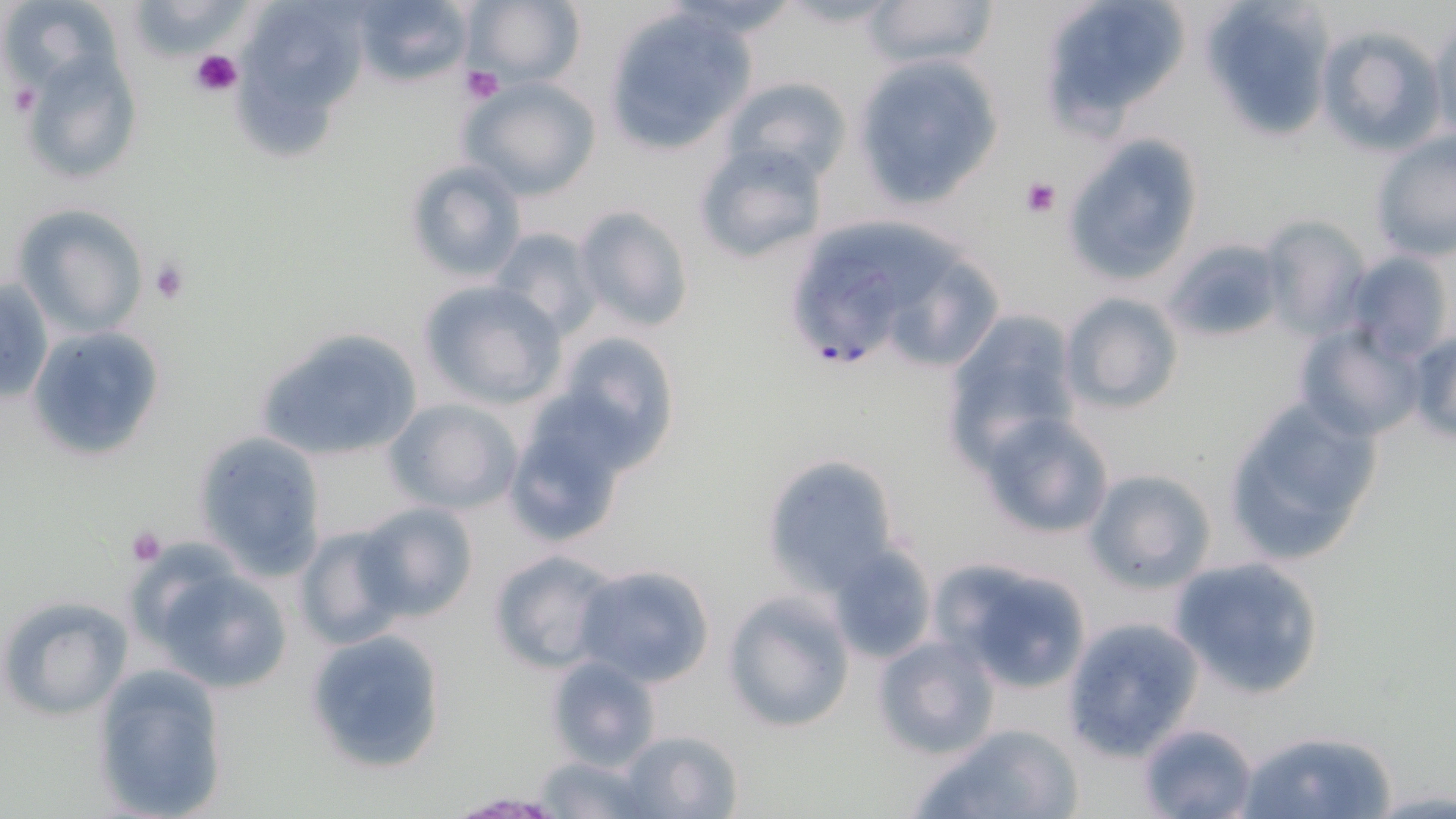
Summary:
  - Coordinate format: approximate bounding boxes as (x1, y1, x2, y2) in pixels
  - Platelet locations: (190, 49, 242, 97), (461, 66, 506, 105), (7, 80, 39, 118), (1019, 176, 1060, 218), (149, 257, 190, 304), (123, 526, 167, 566)
  - Plasmodium falciparum-infected red blood cell locations: (783, 255, 906, 370)
  - Uninfected red blood cell locations: (119, 0, 247, 55), (352, 0, 472, 86), (861, 0, 999, 72), (1039, 0, 1191, 132), (1199, 0, 1339, 143), (462, 1, 586, 87), (3, 5, 126, 90), (602, 10, 752, 154), (253, 11, 371, 102), (1429, 18, 1456, 141), (1314, 22, 1447, 156), (19, 38, 145, 184), (249, 47, 343, 159), (856, 56, 1003, 204), (724, 76, 852, 186), (460, 77, 600, 200), (1061, 133, 1204, 286), (1371, 135, 1456, 262), (692, 139, 828, 266), (402, 158, 527, 286), (12, 204, 150, 340), (573, 204, 695, 332), (815, 214, 964, 314), (1261, 214, 1374, 338), (487, 226, 601, 339), (1165, 239, 1283, 345), (1346, 249, 1454, 362), (902, 259, 1001, 362), (0, 278, 53, 407), (418, 280, 568, 412), (1059, 292, 1183, 413), (943, 311, 1082, 462), (1294, 323, 1423, 443), (27, 326, 165, 460), (253, 326, 427, 462), (1407, 327, 1456, 449), (552, 332, 682, 467), (1221, 395, 1383, 564), (385, 399, 524, 516), (503, 399, 633, 548), (977, 412, 1117, 541), (191, 434, 331, 579), (761, 452, 902, 595), (1084, 469, 1216, 593), (356, 501, 479, 622), (295, 524, 409, 650), (827, 545, 936, 663), (487, 548, 618, 674), (1167, 555, 1326, 699), (933, 559, 1094, 695), (147, 563, 294, 694), (571, 563, 716, 687), (723, 590, 856, 733), (0, 594, 133, 722), (1061, 615, 1204, 761), (304, 629, 449, 775), (872, 634, 1001, 759), (546, 654, 662, 771), (93, 662, 229, 817), (1135, 720, 1259, 819), (916, 723, 1085, 819), (1238, 727, 1398, 819), (614, 730, 742, 817), (533, 754, 650, 818), (444, 793, 568, 818)
  - Slide-level diagnosis: Plasmodium falciparum
  - Magnification: 1000x
  - Modality: optical microscopy
  - Field of view: one of a larger specimen
  - Stain: May-Grünwald-Giemsa
  - Preparation: thin blood film
  - Image size: 1456×819 pixels